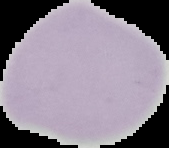 The area outside the segmented cell region is set to black. From a thin blood smear. Result: no malaria parasites detected. Image is 169×148 pixels.